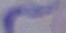
identification = trypanosome
magnification = 1000x
modality = micrograph